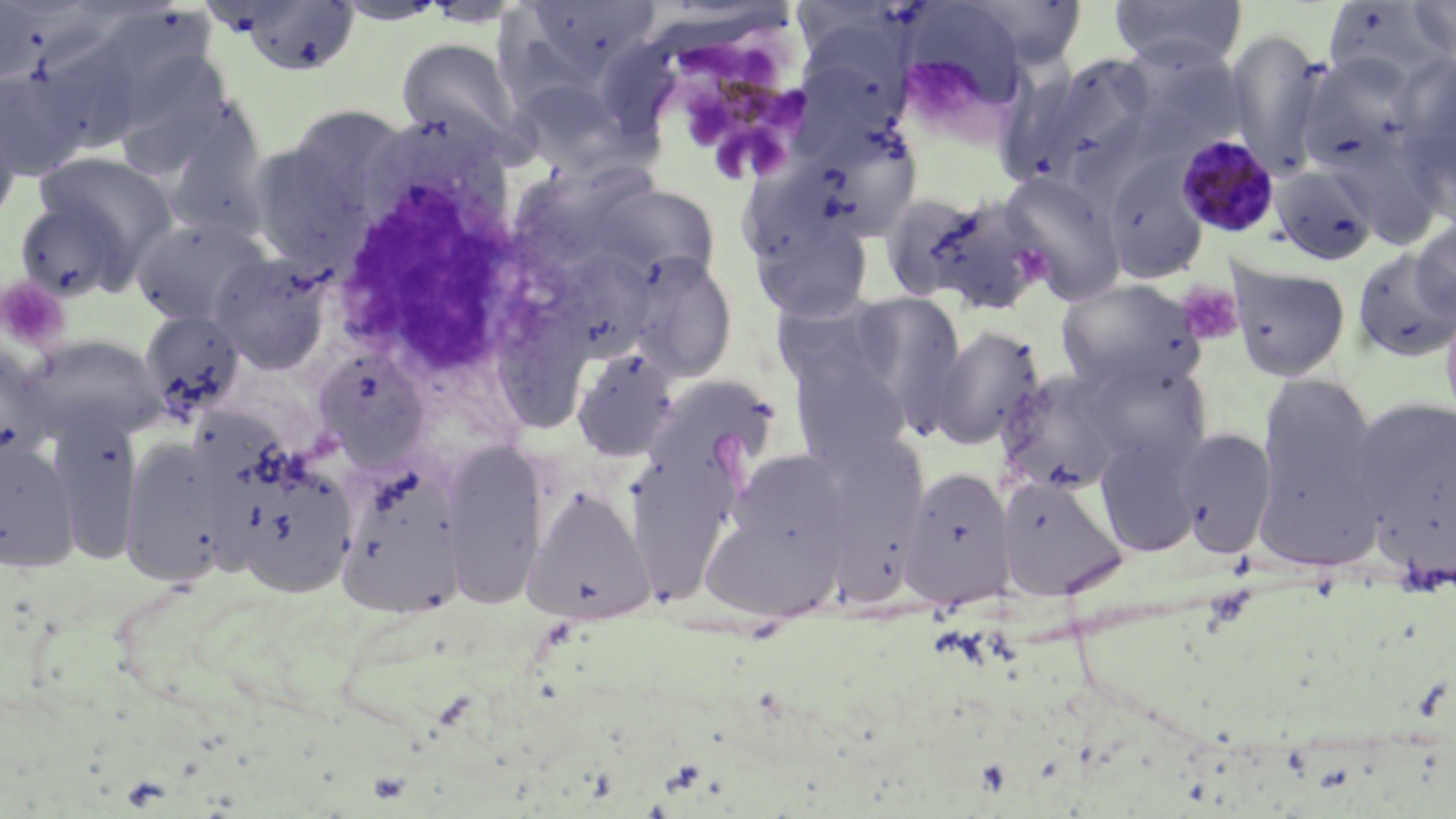 Approximate bounding boxes as named x1/y1/x2/y2 corners in pixels. Platelet locations: (x1=0, y1=277, x2=70, y2=351), (x1=1176, y1=281, x2=1243, y2=345). Plasmodium malariae-infected red blood cell locations: (x1=648, y1=37, x2=820, y2=192), (x1=1174, y1=131, x2=1281, y2=238). White blood cell locations: (x1=330, y1=134, x2=562, y2=386). Uninfected red blood cell locations: (x1=897, y1=0, x2=1039, y2=109), (x1=948, y1=0, x2=1093, y2=73), (x1=1109, y1=0, x2=1248, y2=71), (x1=1407, y1=0, x2=1456, y2=61), (x1=233, y1=1, x2=362, y2=78), (x1=332, y1=1, x2=450, y2=25), (x1=514, y1=1, x2=664, y2=81), (x1=1321, y1=2, x2=1455, y2=86), (x1=106, y1=10, x2=217, y2=125), (x1=31, y1=25, x2=153, y2=155), (x1=1226, y1=29, x2=1332, y2=175), (x1=789, y1=33, x2=912, y2=154), (x1=396, y1=37, x2=527, y2=154), (x1=119, y1=50, x2=225, y2=182), (x1=1297, y1=52, x2=1428, y2=181), (x1=1019, y1=53, x2=1163, y2=192), (x1=1395, y1=54, x2=1456, y2=216), (x1=0, y1=68, x2=95, y2=180), (x1=512, y1=79, x2=631, y2=176), (x1=0, y1=106, x2=24, y2=230), (x1=172, y1=107, x2=273, y2=231), (x1=798, y1=118, x2=926, y2=242), (x1=249, y1=121, x2=399, y2=266), (x1=34, y1=152, x2=176, y2=263), (x1=1101, y1=155, x2=1211, y2=284), (x1=520, y1=160, x2=653, y2=269), (x1=1269, y1=163, x2=1380, y2=267), (x1=997, y1=169, x2=1128, y2=304), (x1=593, y1=182, x2=724, y2=283), (x1=901, y1=192, x2=1052, y2=315), (x1=13, y1=197, x2=137, y2=302), (x1=131, y1=215, x2=271, y2=326), (x1=750, y1=219, x2=874, y2=323), (x1=1412, y1=219, x2=1456, y2=322), (x1=1352, y1=249, x2=1456, y2=363), (x1=551, y1=250, x2=658, y2=361), (x1=209, y1=253, x2=333, y2=374), (x1=624, y1=253, x2=738, y2=383), (x1=1228, y1=261, x2=1351, y2=382), (x1=1055, y1=278, x2=1207, y2=395), (x1=770, y1=291, x2=905, y2=405), (x1=841, y1=291, x2=970, y2=428), (x1=1439, y1=297, x2=1456, y2=431), (x1=138, y1=310, x2=246, y2=426), (x1=929, y1=324, x2=1046, y2=450), (x1=29, y1=335, x2=167, y2=442), (x1=571, y1=346, x2=680, y2=461), (x1=311, y1=349, x2=428, y2=464), (x1=786, y1=350, x2=915, y2=467), (x1=1080, y1=357, x2=1214, y2=476), (x1=996, y1=369, x2=1130, y2=496), (x1=644, y1=374, x2=780, y2=487), (x1=1255, y1=374, x2=1381, y2=554), (x1=1347, y1=398, x2=1456, y2=559), (x1=1174, y1=426, x2=1277, y2=557), (x1=815, y1=431, x2=932, y2=564), (x1=1094, y1=434, x2=1202, y2=557), (x1=442, y1=439, x2=549, y2=606), (x1=0, y1=441, x2=80, y2=572), (x1=625, y1=445, x2=740, y2=598), (x1=122, y1=446, x2=228, y2=587), (x1=732, y1=450, x2=849, y2=553), (x1=899, y1=466, x2=1017, y2=610), (x1=233, y1=472, x2=357, y2=599), (x1=997, y1=476, x2=1127, y2=600), (x1=525, y1=487, x2=655, y2=624), (x1=701, y1=514, x2=840, y2=621). Slide-level diagnosis: Plasmodium malariae. May-Grünwald-Giemsa-stained preparation. Image is 1456×819 pixels. Thin blood film. 1000x magnification. Optical microscopy. One field of a larger specimen.